Classify this cell by malaria status.
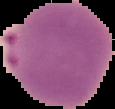
Parasitized.

Image is 115×109 pixels. From a thin blood smear. Segmented cell region on a black background.